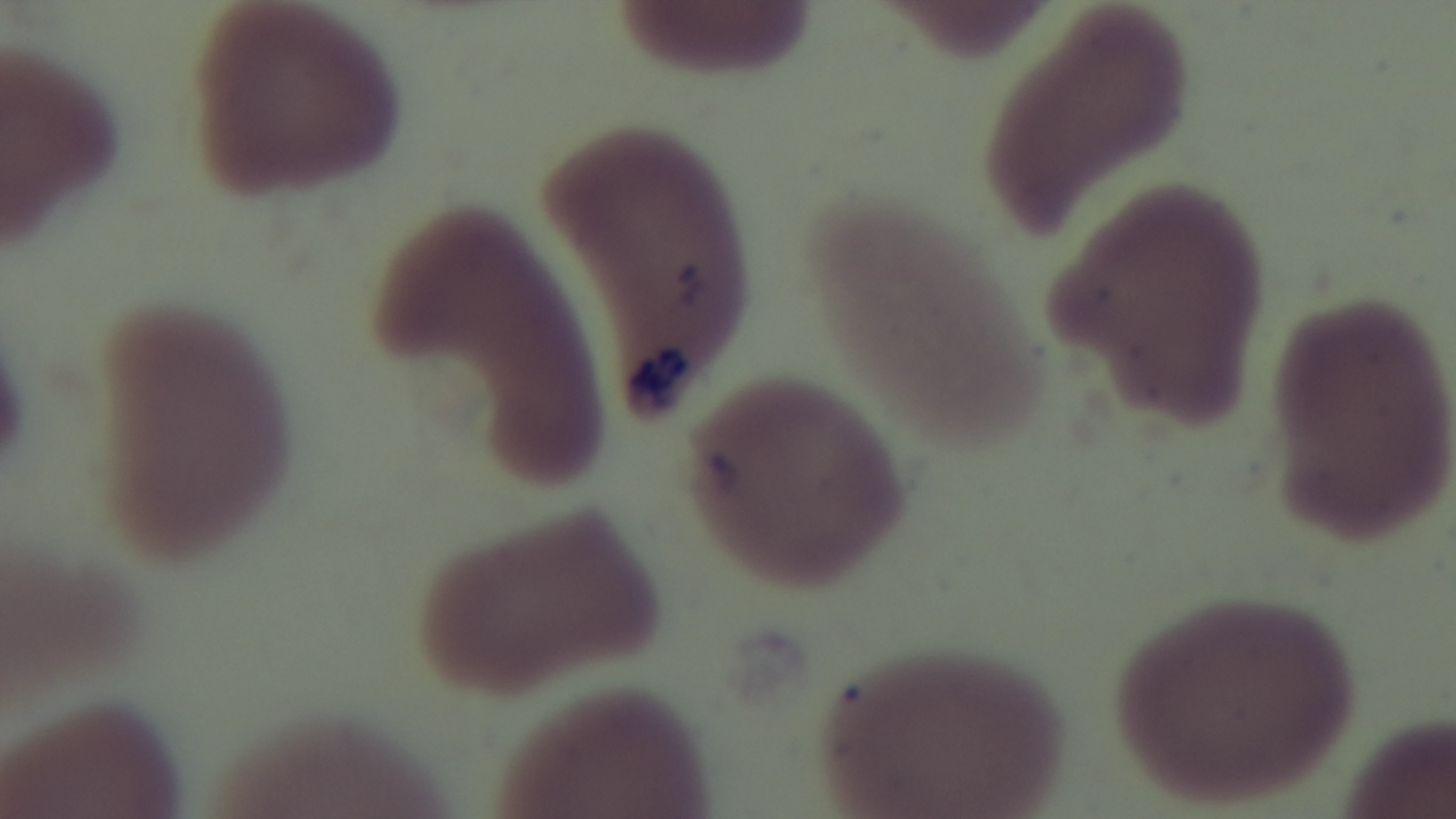
stain = Giemsa
preparation = thin
objective = 100x oil immersion
malaria status = uninfected
modality = light microscopy
capture = mounted 4K digital camera
field of view = one from the slide